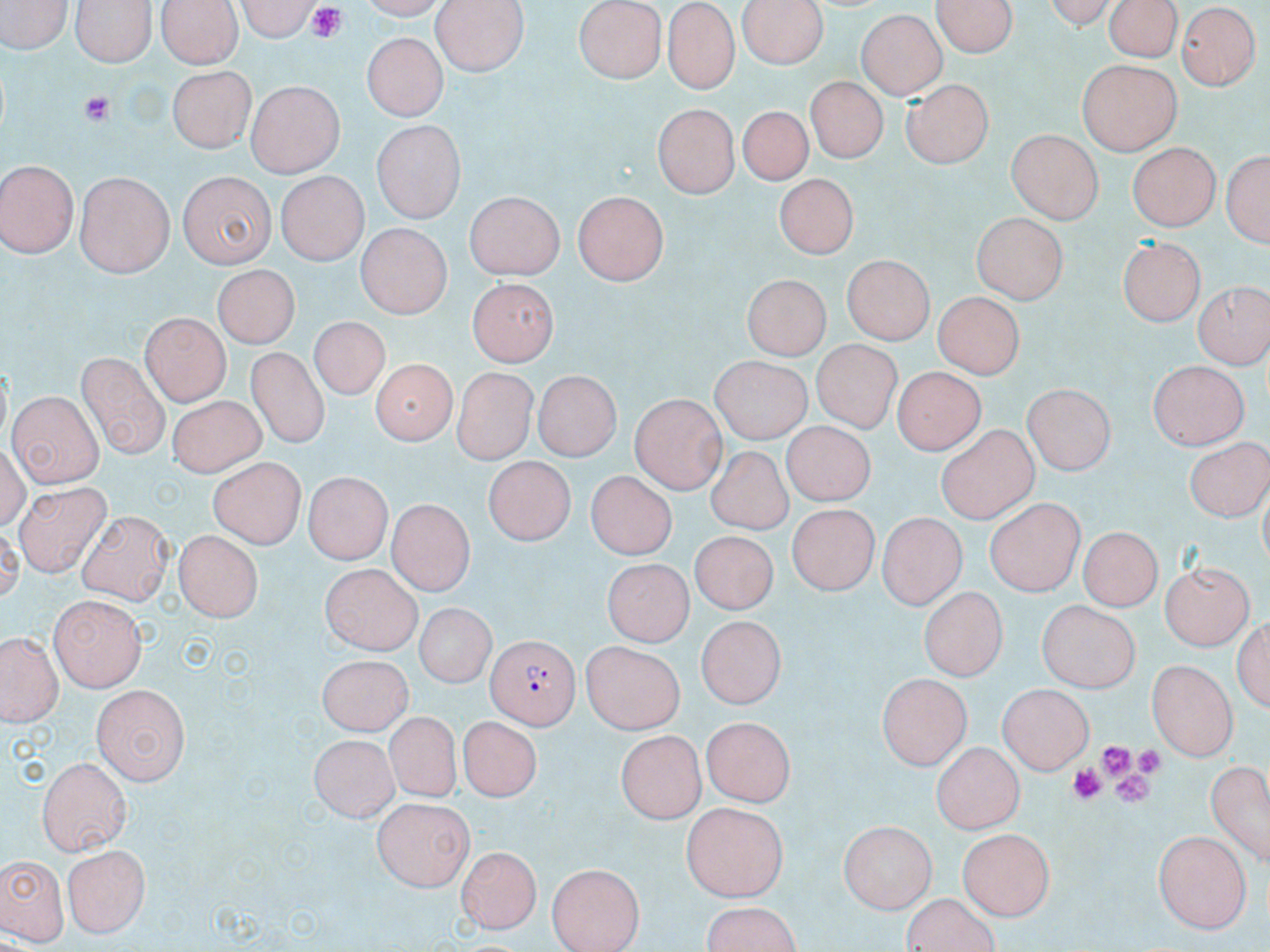

Summary:
  - Coordinate format: approximate bounding boxes as named x1/y1/x2/y2 corners in pixels
  - Platelet locations: (x1=302, y1=4, x2=350, y2=41), (x1=78, y1=90, x2=111, y2=126), (x1=1100, y1=740, x2=1136, y2=776), (x1=1137, y1=747, x2=1163, y2=774), (x1=1068, y1=763, x2=1104, y2=801), (x1=1112, y1=771, x2=1155, y2=804)
  - Uninfected red blood cell locations: (x1=0, y1=0, x2=71, y2=56), (x1=73, y1=0, x2=154, y2=64), (x1=156, y1=0, x2=245, y2=68), (x1=230, y1=0, x2=322, y2=39), (x1=430, y1=0, x2=528, y2=74), (x1=736, y1=0, x2=832, y2=67), (x1=933, y1=0, x2=1020, y2=59), (x1=1109, y1=0, x2=1179, y2=63), (x1=575, y1=2, x2=666, y2=82), (x1=661, y1=3, x2=742, y2=95), (x1=1179, y1=3, x2=1259, y2=91), (x1=857, y1=11, x2=945, y2=99), (x1=364, y1=32, x2=446, y2=123), (x1=1076, y1=59, x2=1183, y2=155), (x1=166, y1=68, x2=258, y2=150), (x1=807, y1=75, x2=888, y2=161), (x1=902, y1=76, x2=998, y2=168), (x1=247, y1=81, x2=345, y2=175), (x1=652, y1=102, x2=742, y2=197), (x1=738, y1=104, x2=813, y2=187), (x1=373, y1=124, x2=464, y2=224), (x1=1006, y1=129, x2=1102, y2=223), (x1=1128, y1=141, x2=1226, y2=232), (x1=1219, y1=142, x2=1270, y2=252), (x1=0, y1=161, x2=79, y2=258), (x1=175, y1=170, x2=277, y2=268), (x1=777, y1=171, x2=863, y2=257), (x1=76, y1=172, x2=175, y2=277), (x1=277, y1=172, x2=366, y2=264), (x1=573, y1=191, x2=671, y2=286), (x1=466, y1=193, x2=563, y2=281), (x1=972, y1=213, x2=1068, y2=302), (x1=356, y1=225, x2=451, y2=316), (x1=1119, y1=236, x2=1208, y2=324), (x1=841, y1=254, x2=932, y2=342), (x1=211, y1=267, x2=299, y2=352), (x1=740, y1=274, x2=834, y2=357), (x1=467, y1=280, x2=556, y2=366), (x1=1194, y1=282, x2=1267, y2=365), (x1=931, y1=292, x2=1027, y2=376), (x1=140, y1=311, x2=230, y2=407), (x1=306, y1=319, x2=387, y2=405), (x1=811, y1=337, x2=911, y2=434), (x1=708, y1=350, x2=816, y2=446), (x1=245, y1=352, x2=330, y2=450), (x1=79, y1=353, x2=171, y2=456), (x1=368, y1=356, x2=455, y2=441), (x1=1148, y1=356, x2=1248, y2=449), (x1=892, y1=368, x2=983, y2=453), (x1=450, y1=370, x2=536, y2=464), (x1=531, y1=372, x2=620, y2=461), (x1=1021, y1=385, x2=1117, y2=474), (x1=9, y1=390, x2=103, y2=486), (x1=167, y1=394, x2=267, y2=472), (x1=629, y1=395, x2=727, y2=492), (x1=779, y1=421, x2=881, y2=508), (x1=935, y1=423, x2=1038, y2=524), (x1=1183, y1=436, x2=1270, y2=518), (x1=704, y1=444, x2=799, y2=535), (x1=482, y1=456, x2=579, y2=541), (x1=208, y1=458, x2=303, y2=549), (x1=583, y1=467, x2=682, y2=564), (x1=304, y1=468, x2=388, y2=563), (x1=16, y1=480, x2=108, y2=575), (x1=984, y1=499, x2=1084, y2=595), (x1=385, y1=501, x2=472, y2=596), (x1=788, y1=505, x2=876, y2=596), (x1=76, y1=508, x2=175, y2=601), (x1=877, y1=510, x2=970, y2=606), (x1=1080, y1=524, x2=1162, y2=609), (x1=175, y1=529, x2=263, y2=619), (x1=689, y1=532, x2=778, y2=615), (x1=601, y1=557, x2=694, y2=644), (x1=1160, y1=561, x2=1254, y2=651), (x1=319, y1=569, x2=421, y2=656), (x1=918, y1=587, x2=1006, y2=680), (x1=49, y1=593, x2=147, y2=690), (x1=1039, y1=602, x2=1139, y2=692), (x1=412, y1=604, x2=495, y2=691), (x1=1234, y1=611, x2=1269, y2=713), (x1=696, y1=616, x2=783, y2=711), (x1=4, y1=633, x2=59, y2=721), (x1=581, y1=640, x2=687, y2=732), (x1=315, y1=655, x2=415, y2=732), (x1=1146, y1=659, x2=1238, y2=761), (x1=875, y1=673, x2=972, y2=772), (x1=999, y1=682, x2=1091, y2=775), (x1=93, y1=686, x2=191, y2=787), (x1=380, y1=707, x2=460, y2=796), (x1=459, y1=714, x2=545, y2=800), (x1=703, y1=716, x2=798, y2=805), (x1=614, y1=730, x2=708, y2=820), (x1=308, y1=733, x2=400, y2=821), (x1=931, y1=740, x2=1024, y2=833), (x1=37, y1=755, x2=132, y2=853), (x1=1207, y1=761, x2=1269, y2=868), (x1=372, y1=797, x2=473, y2=890), (x1=680, y1=802, x2=787, y2=902), (x1=839, y1=820, x2=936, y2=912), (x1=957, y1=828, x2=1057, y2=917), (x1=1154, y1=830, x2=1251, y2=932), (x1=64, y1=844, x2=150, y2=937), (x1=459, y1=846, x2=543, y2=927), (x1=0, y1=853, x2=67, y2=942), (x1=546, y1=859, x2=643, y2=951), (x1=902, y1=894, x2=1003, y2=952), (x1=701, y1=901, x2=804, y2=952)
  - Plasmodium falciparum-infected red blood cell locations: (x1=485, y1=634, x2=583, y2=725)
  - Slide-level diagnosis: Plasmodium falciparum
  - Field of view: one of a larger specimen
  - Preparation: thin blood film
  - Magnification: 1000x
  - Image size: 1270×952 pixels
  - Modality: light microscopy
  - Stain: May-Grünwald-Giemsa